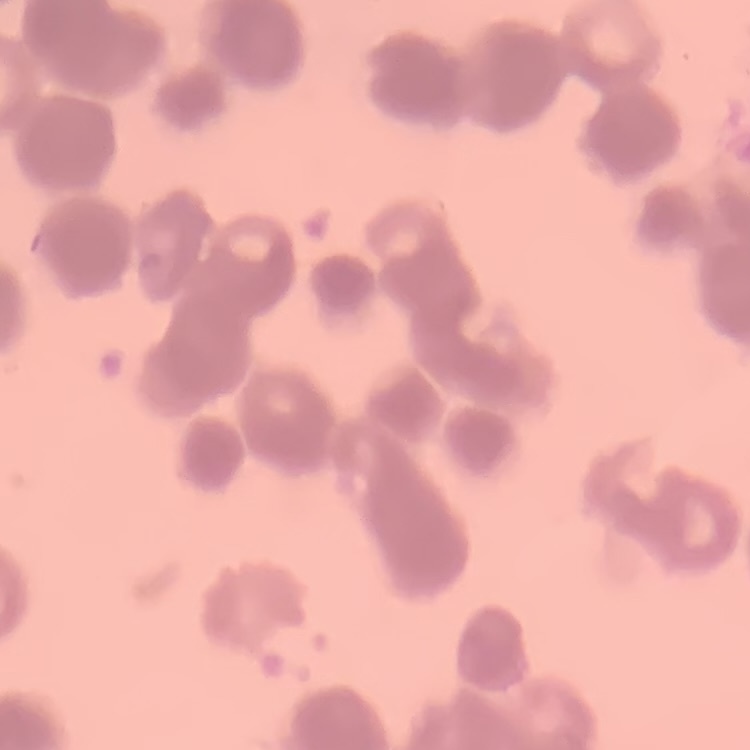

erythrocyte morphology = rouleaux formation
image type = square crop of a larger photomicrograph
stain = Field's or Giemsa
preparation = thin blood smear